State which parasite is depicted.
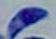
Toxoplasma gondii.

modality: micrograph
magnification: 1000x